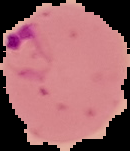
image size = 130×151 pixels
malaria status = parasitized
image type = segmented cell region on a black background
preparation = thin blood film